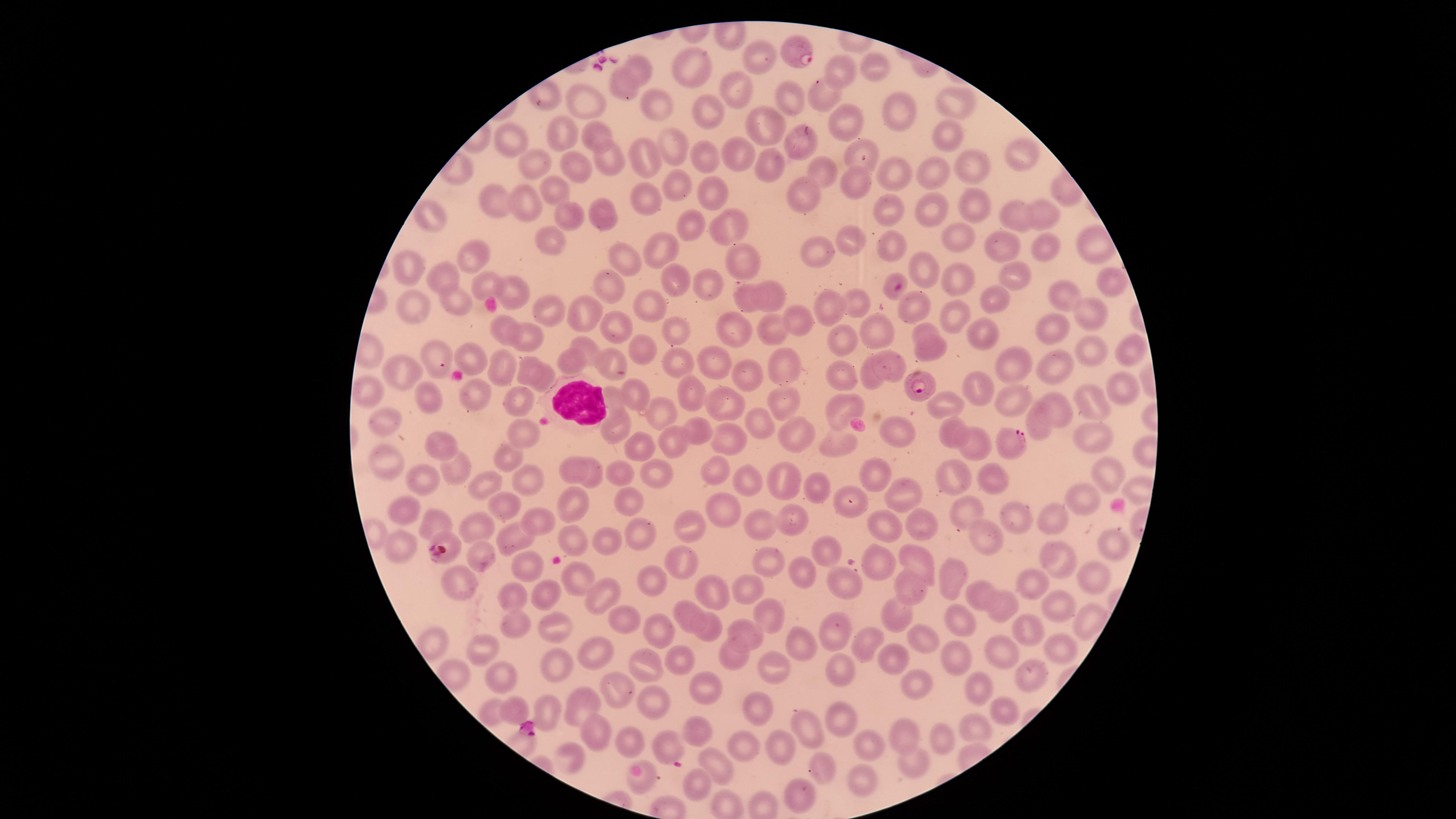
Approximate marker points, in pixels from the top-left corner. Uninfected RBCs: (x=761, y=57), (x=869, y=59), (x=694, y=65), (x=640, y=67), (x=838, y=69), (x=626, y=84), (x=739, y=90), (x=826, y=95), (x=582, y=98), (x=788, y=103), (x=652, y=104), (x=956, y=105), (x=704, y=109), (x=897, y=110), (x=841, y=119), (x=764, y=124), (x=557, y=133), (x=596, y=134), (x=948, y=136), (x=515, y=142), (x=678, y=142), (x=795, y=142), (x=863, y=150), (x=706, y=153), (x=738, y=153), (x=1023, y=153), (x=652, y=154), (x=608, y=155), (x=767, y=164), (x=532, y=165), (x=582, y=168), (x=969, y=168), (x=892, y=169), (x=825, y=170), (x=937, y=174), (x=676, y=182), (x=707, y=187), (x=857, y=187), (x=550, y=189), (x=803, y=193), (x=491, y=202), (x=651, y=203), (x=969, y=203), (x=520, y=205), (x=927, y=208), (x=1006, y=211), (x=886, y=212), (x=1039, y=212), (x=573, y=213), (x=602, y=213), (x=430, y=218), (x=688, y=227), (x=733, y=227), (x=965, y=236), (x=553, y=237), (x=854, y=241), (x=893, y=245), (x=1002, y=247), (x=661, y=250), (x=1052, y=250), (x=469, y=251), (x=819, y=253), (x=745, y=258), (x=630, y=259), (x=922, y=263), (x=414, y=271), (x=1012, y=271), (x=675, y=275), (x=446, y=278), (x=1101, y=279), (x=605, y=281), (x=704, y=281), (x=955, y=283), (x=488, y=286), (x=771, y=289), (x=520, y=292), (x=892, y=292), (x=1061, y=294), (x=455, y=299), (x=748, y=300), (x=991, y=300), (x=860, y=304), (x=913, y=305), (x=646, y=307), (x=420, y=308), (x=828, y=308), (x=553, y=312), (x=585, y=313), (x=946, y=315), (x=1094, y=315), (x=796, y=320), (x=503, y=326), (x=616, y=327), (x=879, y=328), (x=926, y=328), (x=732, y=329), (x=1061, y=330), (x=983, y=331), (x=678, y=332), (x=774, y=333), (x=525, y=336), (x=845, y=337), (x=587, y=346), (x=638, y=349), (x=933, y=350), (x=1090, y=350), (x=1128, y=354), (x=435, y=356), (x=471, y=359), (x=581, y=360), (x=897, y=360), (x=1016, y=360), (x=786, y=361), (x=609, y=362), (x=720, y=362), (x=527, y=365), (x=499, y=367), (x=1054, y=368), (x=681, y=369), (x=403, y=371), (x=845, y=372), (x=746, y=378), (x=870, y=379), (x=541, y=384), (x=1123, y=387), (x=974, y=388), (x=635, y=391), (x=364, y=392), (x=697, y=393), (x=787, y=398), (x=611, y=399), (x=434, y=400), (x=477, y=400), (x=1095, y=400), (x=515, y=404), (x=942, y=404), (x=1012, y=404), (x=842, y=405), (x=1058, y=405), (x=724, y=407), (x=661, y=412), (x=386, y=420), (x=617, y=423), (x=1037, y=423), (x=761, y=426), (x=899, y=429), (x=697, y=430), (x=951, y=434), (x=527, y=435), (x=730, y=436), (x=793, y=436), (x=1086, y=436), (x=672, y=439), (x=837, y=439), (x=963, y=440), (x=640, y=444), (x=439, y=445), (x=506, y=456), (x=388, y=463), (x=456, y=468), (x=574, y=469), (x=783, y=472), (x=868, y=472), (x=1106, y=472), (x=710, y=473), (x=617, y=474), (x=654, y=474), (x=985, y=474), (x=420, y=476), (x=526, y=479), (x=594, y=480), (x=747, y=483), (x=486, y=484), (x=957, y=486), (x=895, y=487), (x=816, y=492), (x=624, y=498), (x=849, y=498), (x=1081, y=499), (x=504, y=503), (x=575, y=504), (x=404, y=506), (x=964, y=508), (x=723, y=511), (x=1012, y=513), (x=436, y=519), (x=530, y=520), (x=1048, y=520), (x=791, y=522), (x=476, y=525), (x=690, y=525), (x=760, y=526), (x=890, y=527), (x=635, y=530), (x=924, y=530), (x=570, y=533), (x=514, y=537), (x=986, y=537), (x=606, y=539), (x=1105, y=540), (x=402, y=545), (x=826, y=551), (x=449, y=552), (x=472, y=553), (x=1051, y=553), (x=680, y=559), (x=768, y=559), (x=878, y=561), (x=915, y=561), (x=519, y=564), (x=798, y=570), (x=950, y=573), (x=578, y=576), (x=1096, y=577), (x=652, y=578), (x=903, y=579), (x=844, y=582), (x=461, y=584), (x=1031, y=586), (x=711, y=588), (x=745, y=588), (x=600, y=591), (x=981, y=592), (x=548, y=593), (x=513, y=595), (x=1054, y=603), (x=1001, y=607), (x=688, y=613), (x=895, y=613), (x=766, y=615), (x=1084, y=615), (x=622, y=619), (x=959, y=619), (x=511, y=624), (x=556, y=624), (x=1022, y=624), (x=713, y=628), (x=835, y=629), (x=660, y=630), (x=747, y=631), (x=870, y=642), (x=928, y=642), (x=800, y=643), (x=1059, y=643), (x=484, y=649), (x=599, y=649), (x=732, y=653), (x=679, y=654), (x=1004, y=654), (x=891, y=655), (x=956, y=658), (x=557, y=660), (x=772, y=665), (x=647, y=666), (x=841, y=671), (x=501, y=676), (x=1025, y=679), (x=971, y=682), (x=917, y=686), (x=615, y=687), (x=701, y=689), (x=588, y=703), (x=759, y=703), (x=656, y=704), (x=512, y=708), (x=548, y=711), (x=1003, y=711), (x=837, y=714), (x=808, y=726), (x=975, y=727), (x=594, y=729), (x=696, y=732), (x=907, y=733), (x=936, y=736), (x=866, y=738), (x=625, y=740), (x=664, y=745), (x=778, y=746), (x=743, y=747), (x=570, y=755), (x=913, y=760), (x=824, y=764), (x=718, y=766), (x=643, y=776), (x=860, y=776), (x=694, y=779), (x=801, y=790). WBCs: (x=573, y=398). Parasitized RBCs: (x=797, y=55), (x=919, y=383), (x=1012, y=443). Giemsa-stained preparation. Thin smear of blood. Species: Plasmodium falciparum. The visible region is circular. Image is 1456×819 pixels. Smartphone photograph through the microscope eyepiece. Presence: malaria parasites detected. Single field of view.